Assess for Plasmodium parasites.
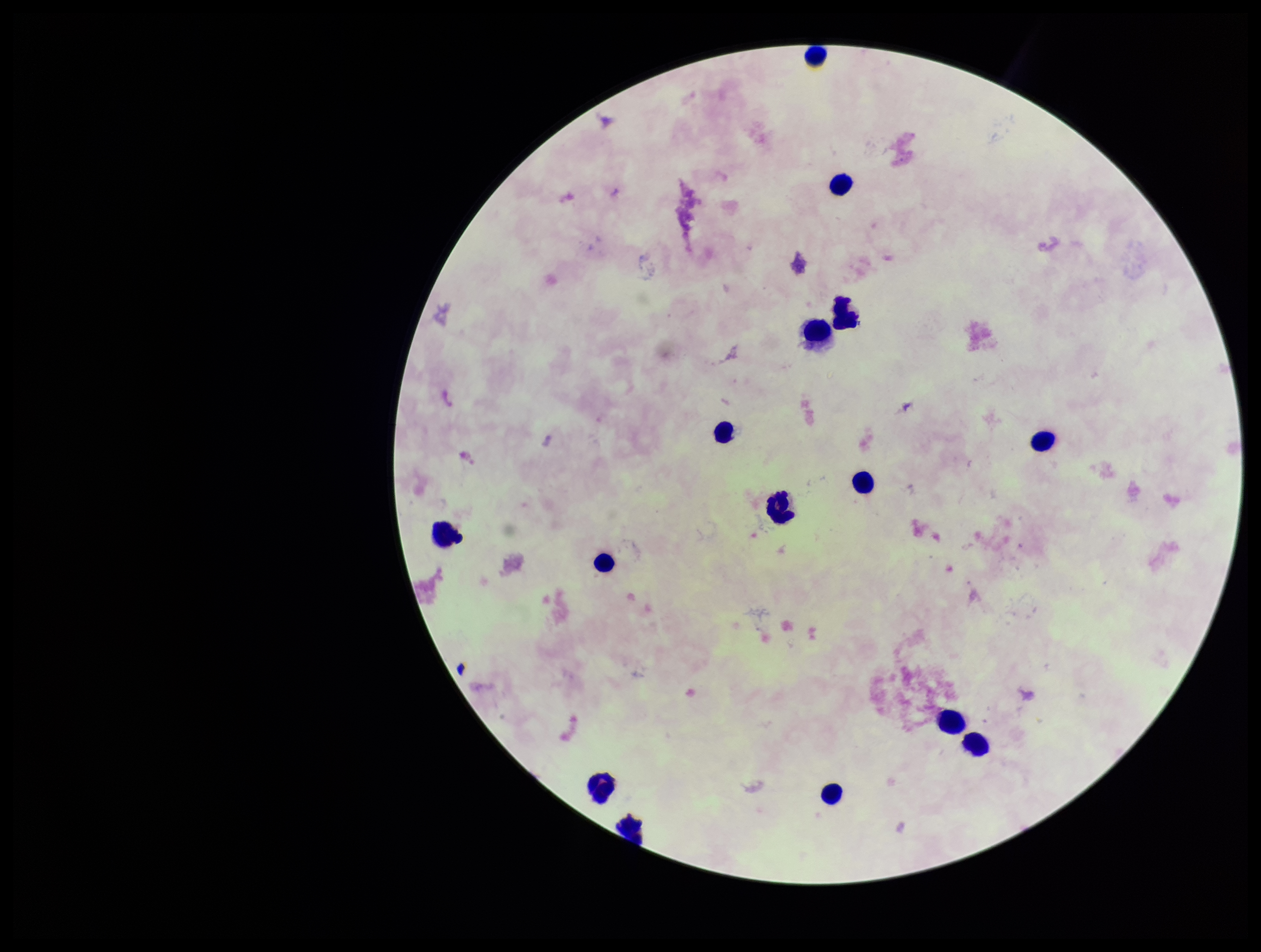

None identified.

patient_malaria_status: negative
stain: Giemsa
leukocyte_count: 15
preparation: thick smear
field_of_view: single
image_size: 1261×952 pixels
parasite_count: 0
capture: smartphone photograph through the microscope eyepiece